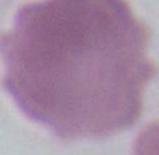

Summary:
  - Magnification: 1000x
  - Modality: photomicrograph
  - Identification: red blood cell